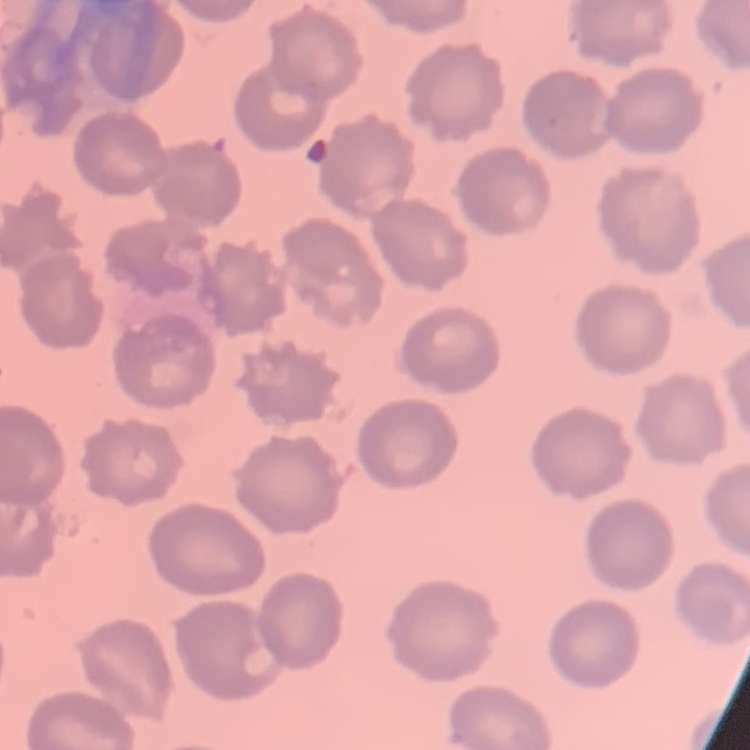
{
  "erythrocyte_morphology": "no rouleaux formation",
  "preparation": "thin blood smear",
  "image_type": "square crop of a larger photomicrograph",
  "stain": "Field's or Giemsa"
}